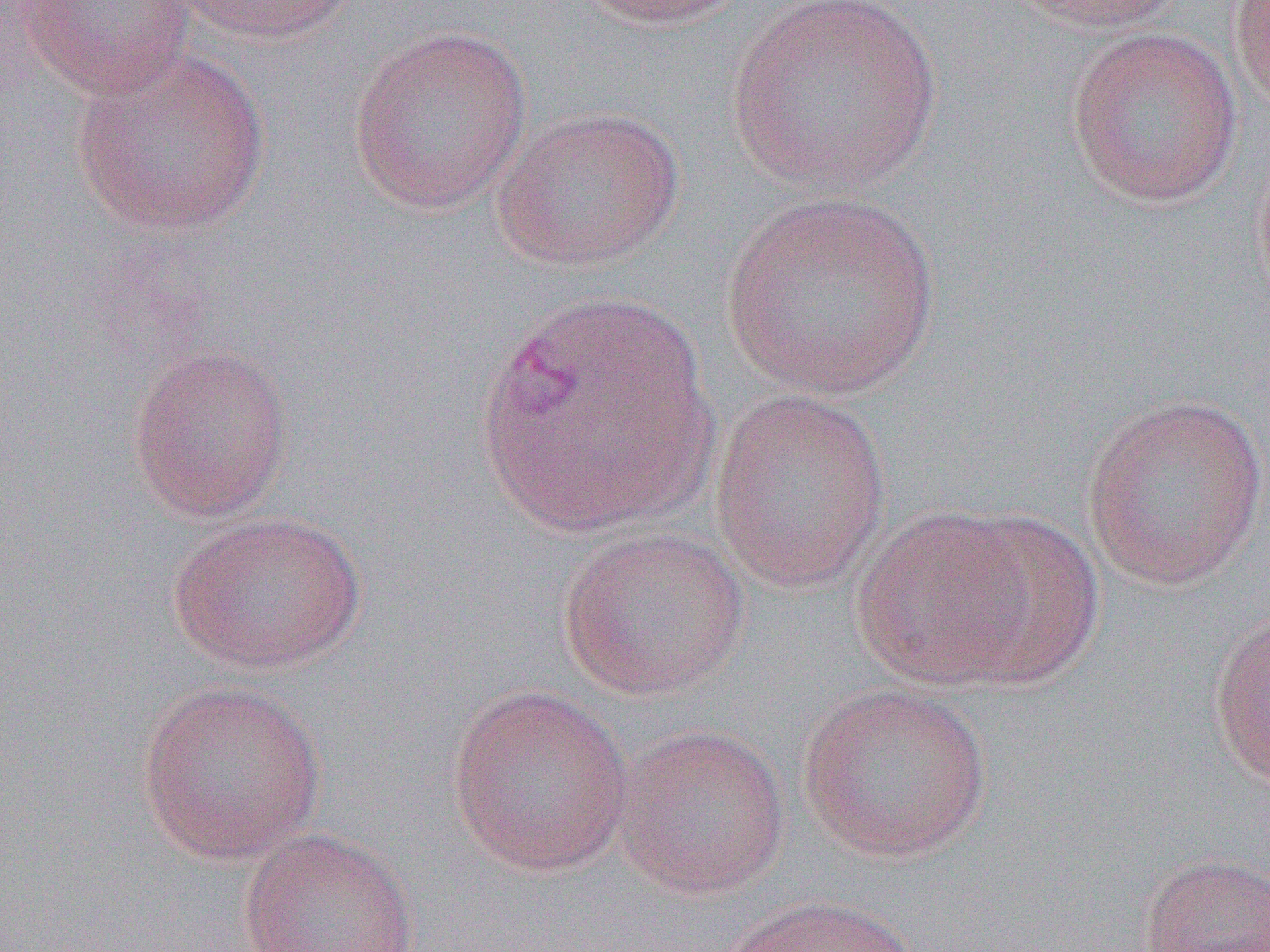
Summary:
  - Coordinate format: approximate bounding boxes as (x1,y1)-(x2,y2) corner pairs in pixels
  - Uninfected red blood cell locations: (168,0)-(363,44), (570,0)-(751,31), (722,0)-(945,195), (1003,0)-(1189,35), (1228,0)-(1270,114), (15,1)-(197,99), (348,26)-(533,214), (1064,26)-(1243,209), (69,46)-(271,235), (490,105)-(687,272), (1250,133)-(1270,322), (722,191)-(942,401), (473,287)-(719,542), (127,343)-(294,523), (708,390)-(892,595), (1079,392)-(1269,592), (850,505)-(1041,691), (166,510)-(367,675), (944,510)-(1105,686), (556,524)-(750,701), (1206,607)-(1270,790), (135,678)-(327,864), (797,681)-(994,862), (445,683)-(636,878), (613,723)-(791,899), (237,827)-(421,952), (1139,852)-(1270,952), (718,894)-(924,952)
  - Slide-level diagnosis: Plasmodium vivax
  - Image size: 1270×952 pixels
  - Magnification: 1000x
  - Field of view: one of a larger specimen
  - Preparation: thin blood film
  - Modality: light microscopy